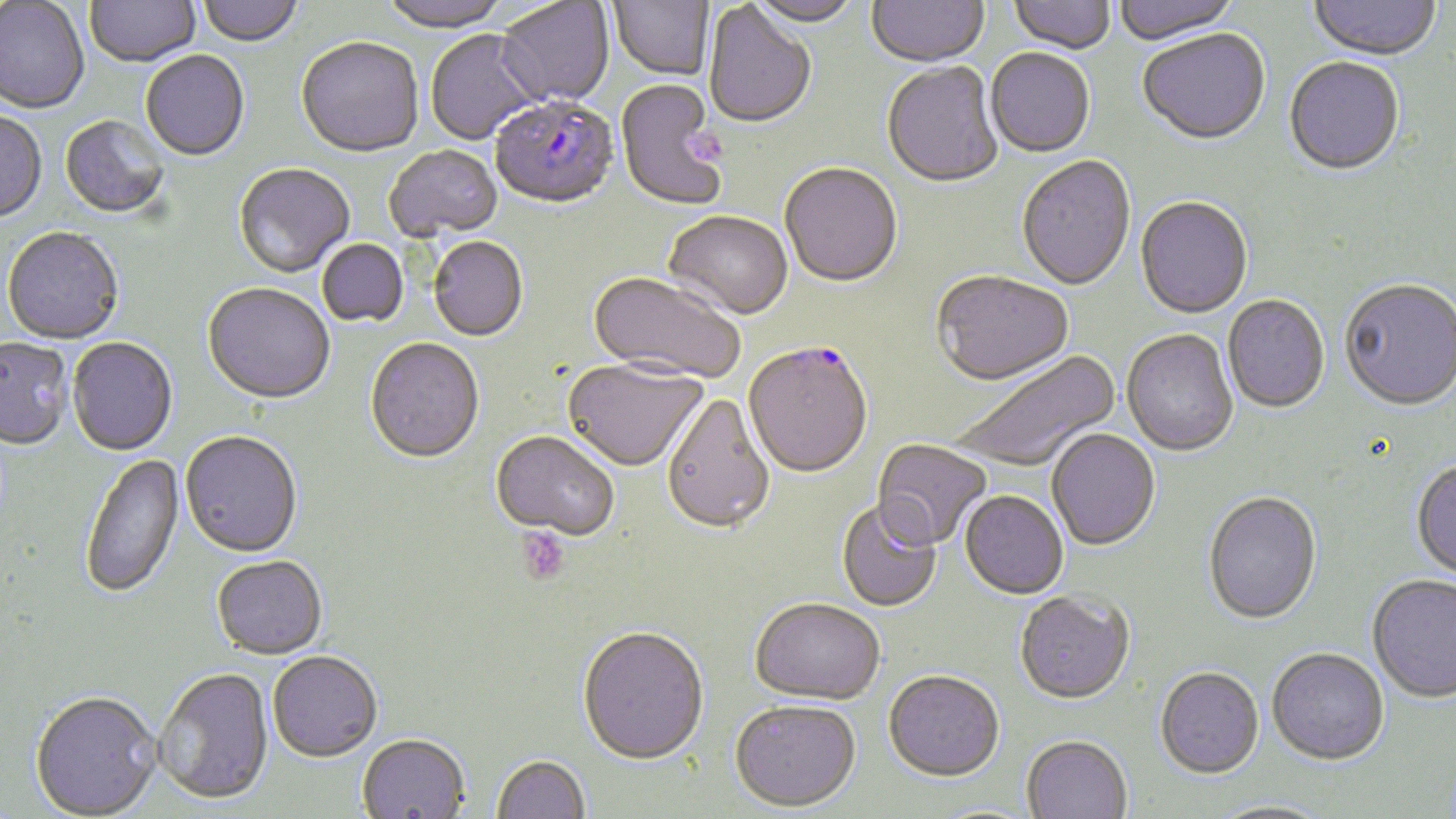

slide-level diagnosis = Plasmodium falciparum
image size = 1456×819 pixels
Plasmodium falciparum-infected red blood cell locations = approximate bounding boxes as (x1,y1)-(x2,y2) corner pairs in pixels: (490,97)-(619,212), (743,344)-(873,482)
magnification = 1000x
stain = May-Grünwald-Giemsa
platelet locations = approximate bounding boxes as (x1,y1)-(x2,y2) corner pairs in pixels: (690,128)-(729,170), (515,527)-(570,585)
preparation = thin blood film
field of view = single
uninfected red blood cell locations = approximate bounding boxes as (x1,y1)-(x2,y2) corner pairs in pixels: (85,0)-(201,70), (197,0)-(303,48), (378,0)-(512,35), (608,0)-(714,82), (746,0)-(860,29), (866,0)-(989,70), (1008,0)-(1116,57), (1114,0)-(1240,47), (1309,0)-(1442,64), (0,1)-(90,116), (495,1)-(615,109), (703,3)-(817,130), (425,30)-(544,146), (1138,31)-(1271,148), (296,40)-(423,160), (985,50)-(1095,159), (141,52)-(249,163), (1283,59)-(1405,178), (882,63)-(1004,190), (615,81)-(730,212), (0,112)-(47,225), (60,117)-(169,220), (385,147)-(503,242), (1017,157)-(1136,292), (780,164)-(903,290), (234,165)-(354,279), (1135,198)-(1253,321), (662,213)-(792,323), (2,229)-(124,346), (428,238)-(528,343), (318,239)-(408,328), (932,272)-(1074,388), (586,273)-(743,386), (1339,281)-(1455,414), (203,284)-(334,406), (1222,296)-(1330,415), (1122,330)-(1239,458), (1,339)-(73,453), (67,339)-(178,457), (365,339)-(484,466), (949,349)-(1122,474), (562,361)-(707,474), (661,395)-(775,539), (1046,430)-(1160,553), (180,433)-(302,560), (490,433)-(618,543), (871,439)-(991,552), (81,453)-(186,601), (1410,461)-(1456,583), (959,493)-(1068,601), (1203,494)-(1322,627), (836,501)-(942,613), (212,557)-(328,662), (1367,576)-(1456,706), (1014,593)-(1135,707), (750,601)-(885,707), (577,629)-(709,768), (1267,650)-(1389,768), (267,654)-(382,765), (154,670)-(274,808), (1155,670)-(1264,782), (883,673)-(1005,785), (29,694)-(162,819), (729,704)-(862,815), (356,736)-(470,819), (1021,738)-(1132,819), (491,756)-(590,819), (1206,801)-(1333,819)
modality = light microscopy